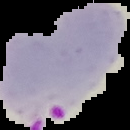 The area outside the segmented cell region is set to black. From a thin blood film. Result: malaria parasites identified. Image is 130×130 pixels.